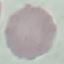
Summary:
  - Result: no malaria parasites seen
  - Preparation: thin blood film
  - Capture: smartphone through the microscope eyepiece
  - Image type: cell patch, automatically extracted from a larger field of view and resized to 64 × 64 pixels
  - Stain: Giemsa